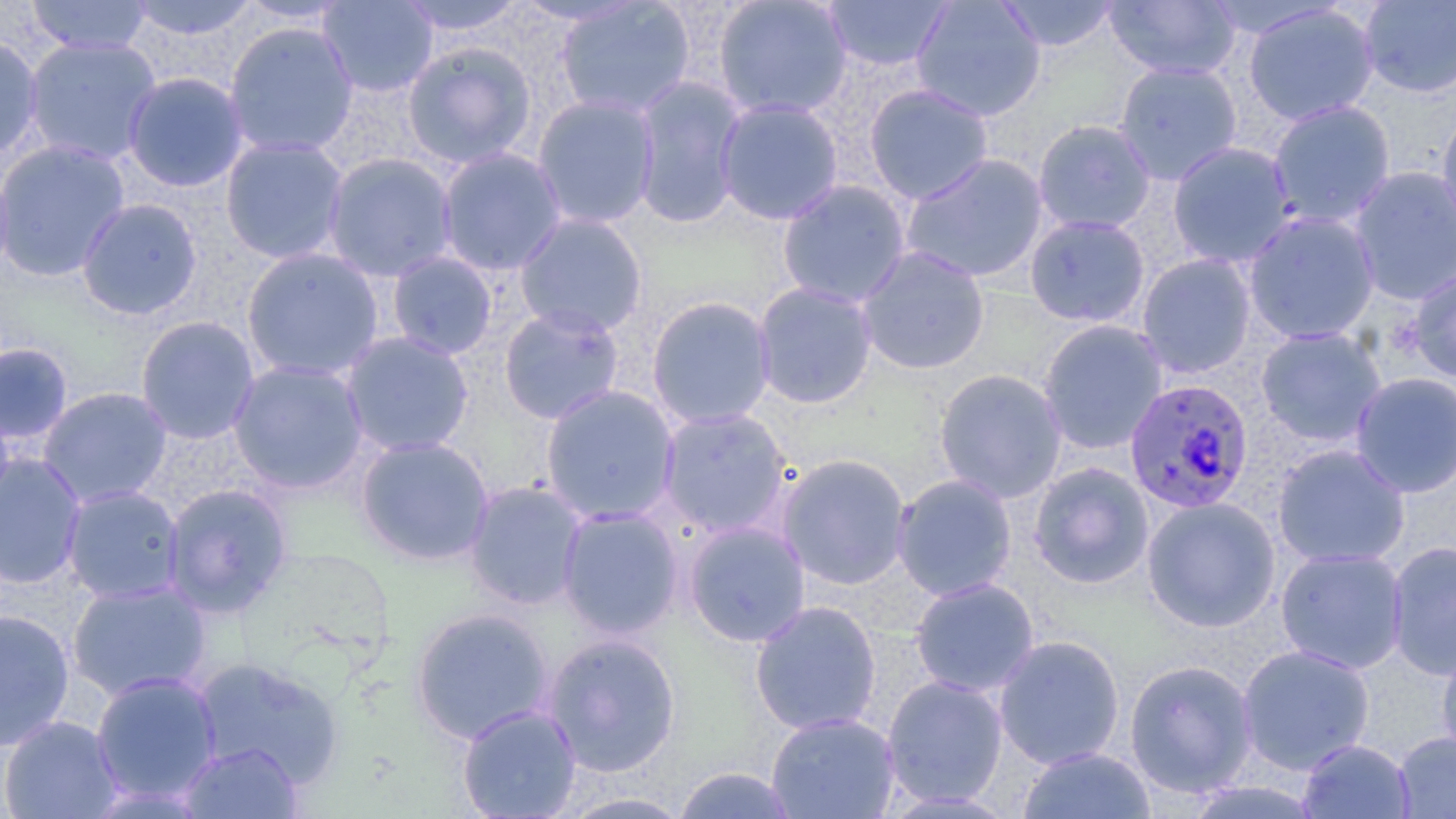

Plasmodium falciparum-infected red blood cell locations = approximate bounding boxes as (x1,y1)-(x2,y2) corner pairs in pixels: (1124,378)-(1255,514)
slide-level diagnosis = Plasmodium falciparum
modality = light microscopy
field of view = single
preparation = thin blood film
uninfected red blood cell locations = approximate bounding boxes as (x1,y1)-(x2,y2) corner pairs in pixels: (26,0)-(152,57), (125,0)-(261,41), (317,0)-(438,98), (395,0)-(527,38), (712,0)-(852,120), (911,0)-(1046,122), (995,0)-(1121,52), (1103,0)-(1241,81), (554,1)-(696,119), (822,1)-(953,72), (1359,1)-(1456,98), (1242,4)-(1379,127), (223,21)-(359,158), (0,34)-(44,161), (22,36)-(162,166), (402,41)-(538,169), (1114,61)-(1243,185), (122,71)-(250,193), (630,75)-(748,229), (864,83)-(994,205), (532,94)-(661,229), (715,98)-(844,225), (1267,100)-(1396,228), (1436,108)-(1456,242), (1032,119)-(1156,234), (220,137)-(350,265), (0,139)-(131,282), (1167,142)-(1296,268), (436,146)-(566,275), (322,152)-(458,282), (900,152)-(1050,284), (0,157)-(16,286), (1348,165)-(1456,306), (776,179)-(912,308), (76,198)-(203,321), (1242,211)-(1380,345), (513,213)-(649,338), (1024,214)-(1150,328), (856,246)-(991,375), (240,247)-(385,382), (386,251)-(499,361), (1137,253)-(1257,378), (1407,264)-(1456,383), (753,282)-(878,409), (646,295)-(776,429), (498,304)-(625,425), (135,315)-(260,444), (1038,319)-(1168,454), (1256,326)-(1386,447), (340,331)-(475,457), (0,342)-(74,449), (227,359)-(370,494), (933,368)-(1068,503), (1351,371)-(1456,498), (540,384)-(680,525), (37,386)-(173,507), (657,407)-(794,538), (355,435)-(494,566), (1272,444)-(1410,568), (776,452)-(912,590), (0,453)-(87,590), (1028,462)-(1154,589), (891,473)-(1018,602), (464,480)-(588,610), (162,483)-(292,617), (61,485)-(185,604), (1141,497)-(1281,632), (557,505)-(684,639), (683,520)-(811,647), (1386,541)-(1456,680), (1275,548)-(1409,674), (909,577)-(1040,697), (66,579)-(211,701), (750,600)-(882,735), (411,606)-(555,745), (0,608)-(74,751), (541,632)-(682,777), (993,634)-(1125,770), (1437,641)-(1456,764), (1236,644)-(1375,774), (994,648)-(1258,780), (192,657)-(345,789), (1124,659)-(1258,798), (90,671)-(223,807), (881,675)-(1009,808), (457,704)-(581,818), (766,712)-(900,818), (0,715)-(123,819), (1394,731)-(1456,818), (1298,739)-(1415,819), (178,741)-(303,818), (1017,746)-(1157,819), (671,766)-(800,818), (1183,780)-(1324,819), (554,791)-(696,818)
magnification = 1000x
image size = 1456×819 pixels
stain = May-Grünwald-Giemsa